Describe the morphology of the erythrocytes.
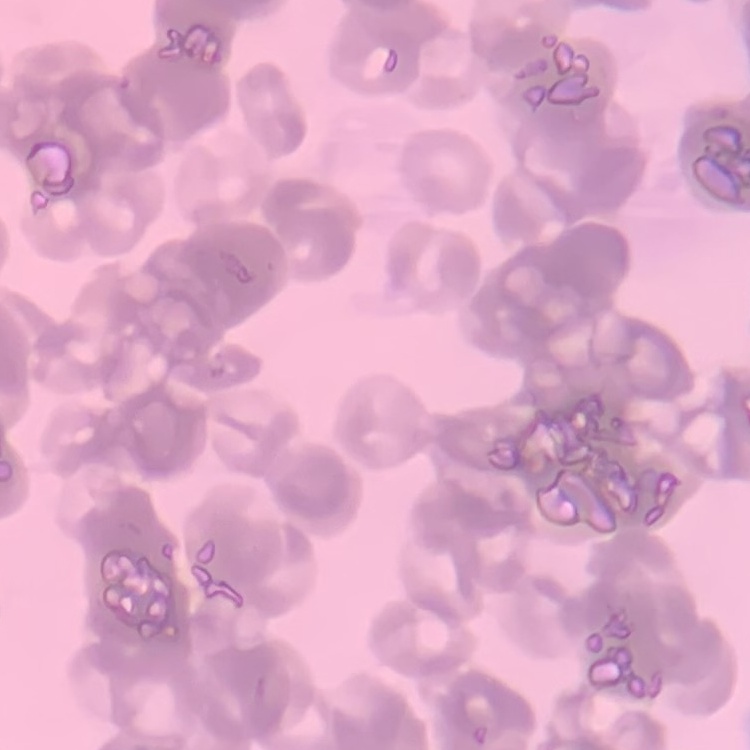
They show rouleaux formation.

Field's or Giemsa stain. Square crop of a larger photomicrograph. Thin peripheral smear.